Name the parasite shown.
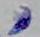

This is Toxoplasma gondii.

Summary:
  - Modality: photomicrograph
  - Magnification: 1000x